Rate the background quality.
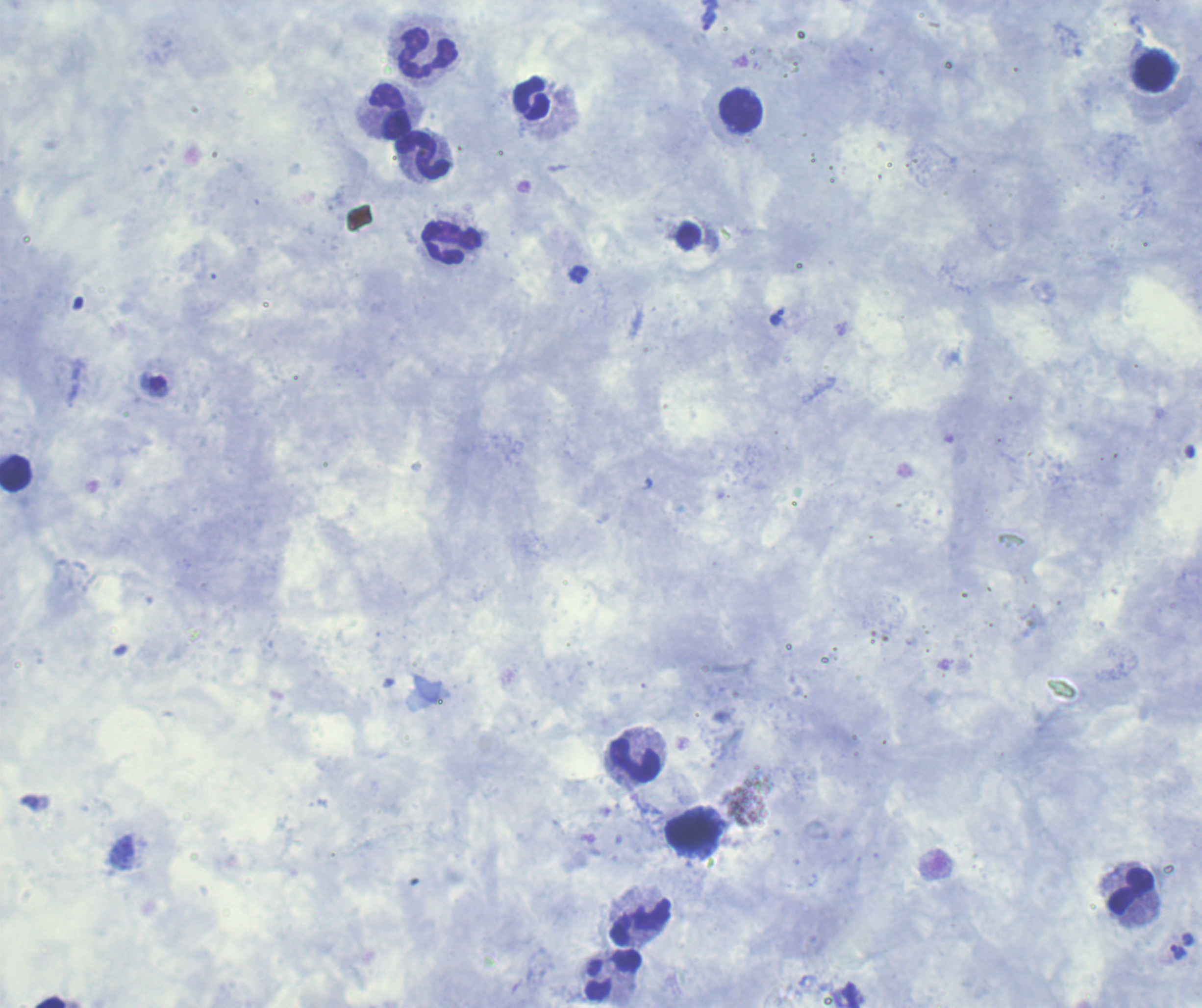

Satisfactory.

{
  "preparation": "thick blood smear",
  "coloration_quality": "good",
  "leukocyte_locations": "approximate centers as (x, y) in pixels: (427, 51), (1152, 70), (531, 98), (740, 110), (388, 111), (422, 154), (452, 243), (15, 473), (634, 760), (694, 831), (1130, 891), (641, 922), (613, 974)",
  "context": "previously used in a real diagnosis",
  "magnification": "100x",
  "result": "malaria parasites detected",
  "image_size": "1202×1008 pixels",
  "field_of_view": "one from this slide",
  "trophozoite_locations": "approximate centers as (x, y) in pixels: (708, 22), (579, 275), (777, 316), (1178, 952)",
  "stain": "Romanowsky"
}